Identify the blood parasite species.
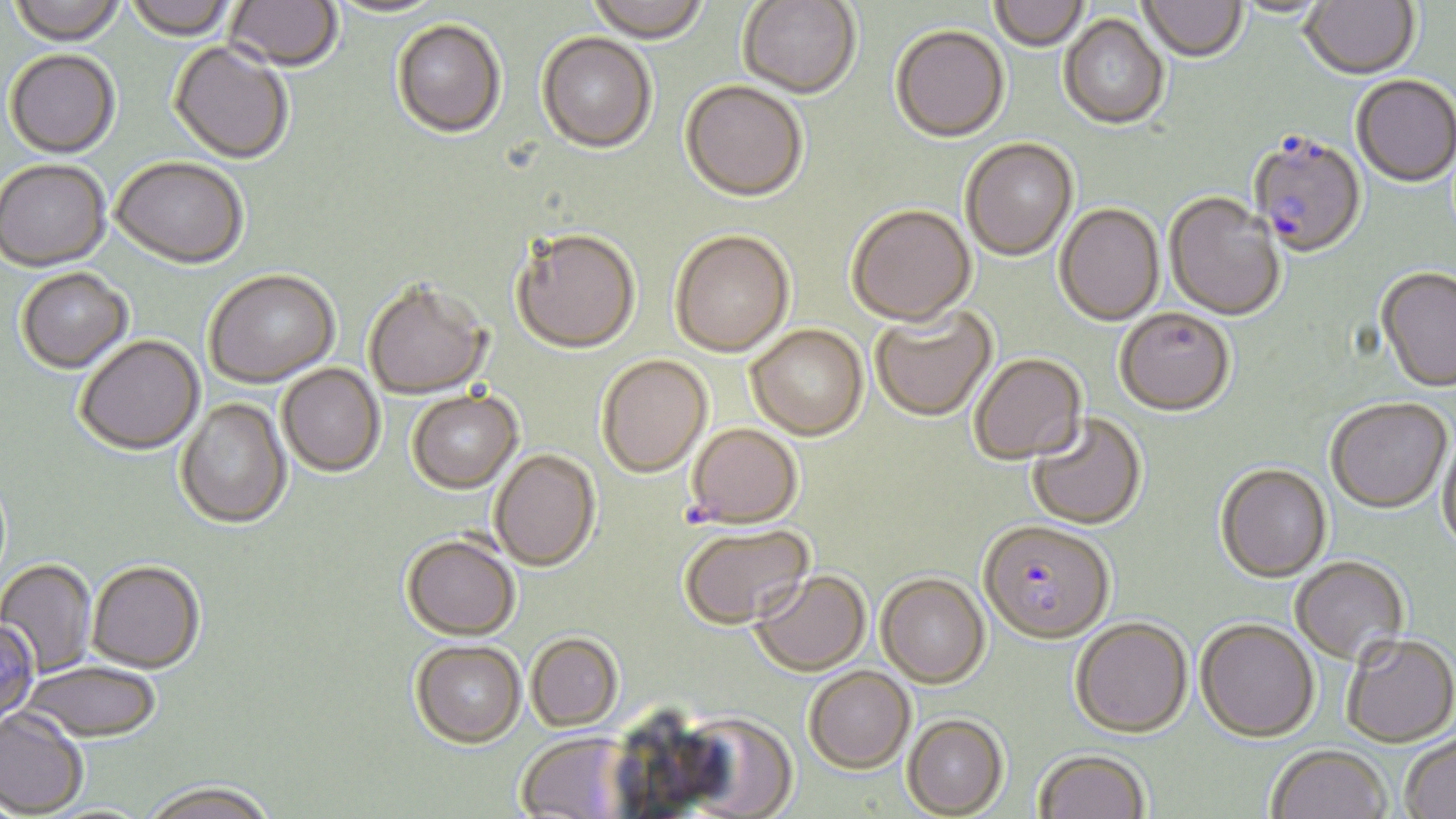
Plasmodium falciparum.

Approximate bounding boxes as (x1,y1)-(x2,y2) corner pairs in pixels. Plasmodium falciparum-infected red blood cell locations: (1247,136)-(1367,261), (978,524)-(1115,648). Uninfected red blood cell locations: (7,0)-(126,49), (124,0)-(238,43), (223,0)-(343,75), (989,0)-(1089,53), (1138,0)-(1247,65), (1231,0)-(1332,20), (1300,0)-(1421,83), (325,1)-(447,19), (585,1)-(710,47), (738,1)-(861,102), (1058,16)-(1169,133), (392,22)-(506,142), (890,28)-(1010,146), (536,34)-(656,156), (168,43)-(292,166), (5,52)-(120,161), (1351,77)-(1456,190), (679,83)-(808,206), (960,140)-(1078,263), (111,159)-(248,272), (0,162)-(111,274), (1164,194)-(1286,323), (1054,205)-(1165,328), (847,207)-(977,331), (512,232)-(641,357), (670,234)-(794,360), (1376,269)-(1456,395), (16,270)-(134,376), (205,272)-(340,390), (364,284)-(491,402), (871,305)-(999,424), (1114,311)-(1235,419), (746,327)-(869,443), (76,337)-(205,458), (970,354)-(1088,467), (597,357)-(712,480), (277,365)-(385,479), (407,392)-(524,497), (175,399)-(292,532), (1326,401)-(1453,516), (1026,414)-(1147,532), (686,425)-(802,531), (1437,433)-(1456,555), (490,451)-(601,574), (1215,466)-(1332,585), (679,526)-(814,631), (401,537)-(519,642), (1292,559)-(1409,669), (0,560)-(96,678), (87,564)-(205,676), (750,571)-(871,677), (876,575)-(990,690), (1070,620)-(1193,740), (1195,621)-(1319,745), (526,634)-(623,731), (1342,637)-(1456,750), (410,641)-(526,749), (22,665)-(161,746), (803,667)-(915,775), (678,707)-(799,816), (0,710)-(87,818), (902,715)-(1008,818), (1400,732)-(1456,819), (516,733)-(635,819), (1267,747)-(1392,819), (1033,751)-(1150,819), (141,786)-(279,819). Optical microscopy. Thin blood film. One field of a larger specimen. Captured at 1000x magnification. May-Grünwald-Giemsa stain. Image is 1456×819 pixels.